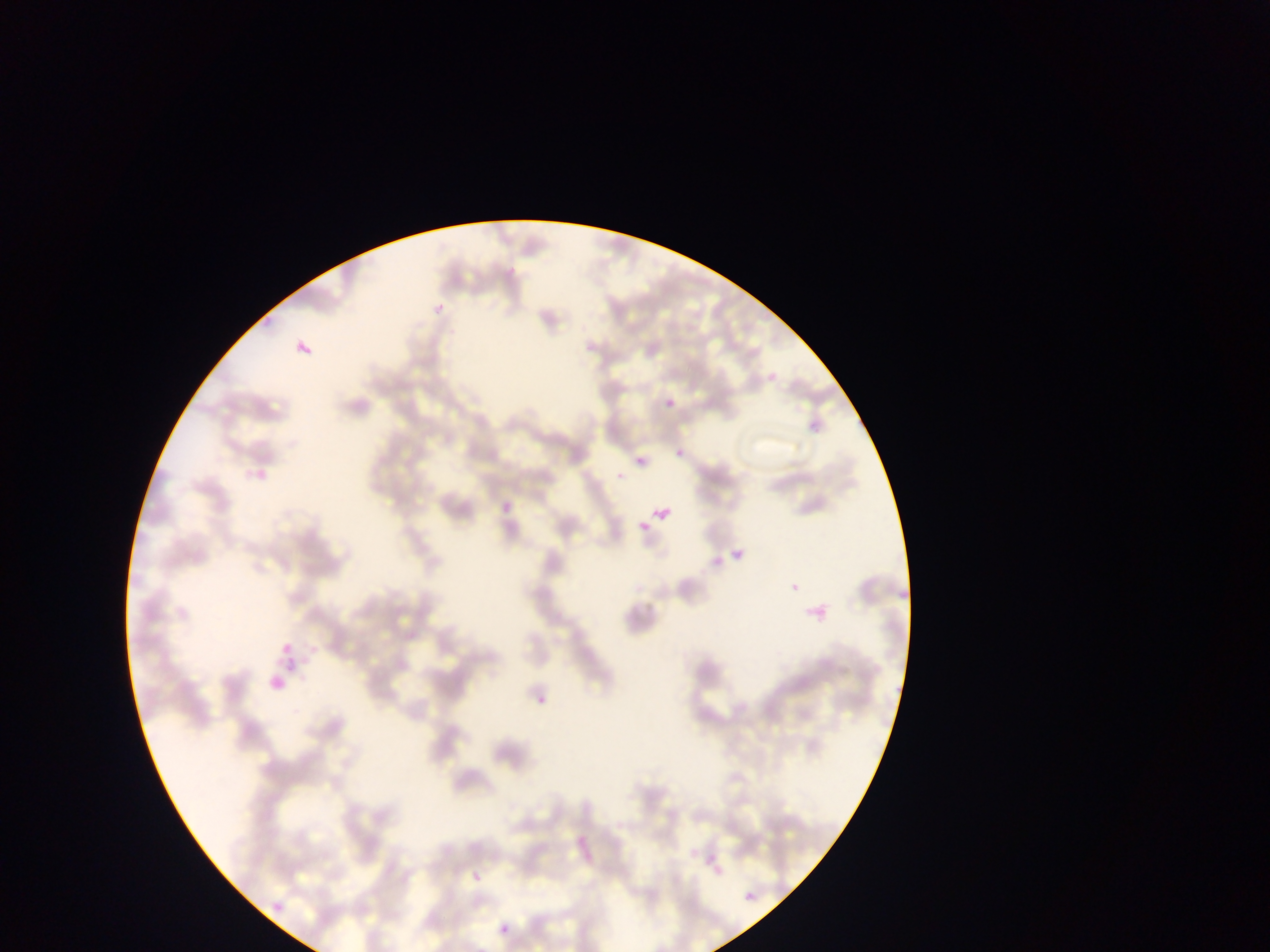

Approximate bounding boxes as left top right bottom in pixels. Plasmodium parasite locations: 428 301 446 315; 296 326 319 358; 663 396 676 409; 674 437 701 460; 635 456 647 467; 615 470 627 482; 653 505 670 521; 639 521 649 533; 730 550 741 564; 781 576 800 599; 272 646 304 659; 283 659 301 685; 534 695 550 717; 791 818 806 833; 689 849 698 859; 472 872 481 882; 745 892 753 900; 499 923 510 934. Image is 1270×952 pixels. Thin blood smear. Collected in Ghana. Photographed through a microscope with a mobile-phone camera. One field of view.